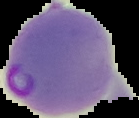 Image is 139×118 pixels. From a thin blood smear. Malaria status: parasitized. The area outside the segmented cell region is set to black.